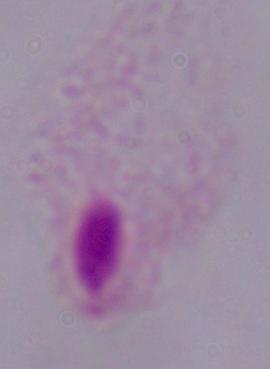

Summary:
  - Identification: trichomonad
  - Magnification: 1000x
  - Modality: micrograph